Assess the morphology of the erythrocytes.
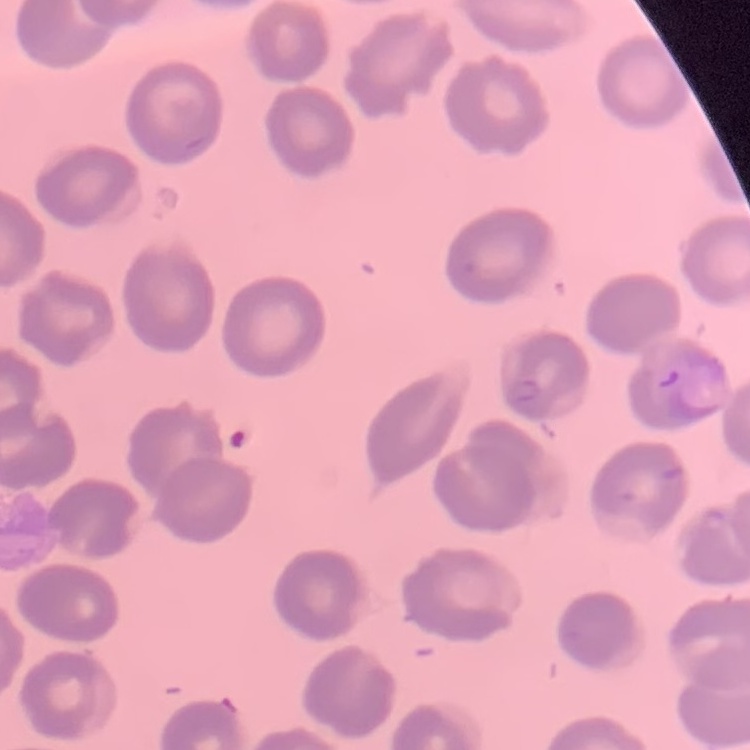
They show no rouleaux formation.

Summary:
  - Stain: Field's or Giemsa
  - Image type: one tile cut from a larger photomicrograph
  - Preparation: thin blood film